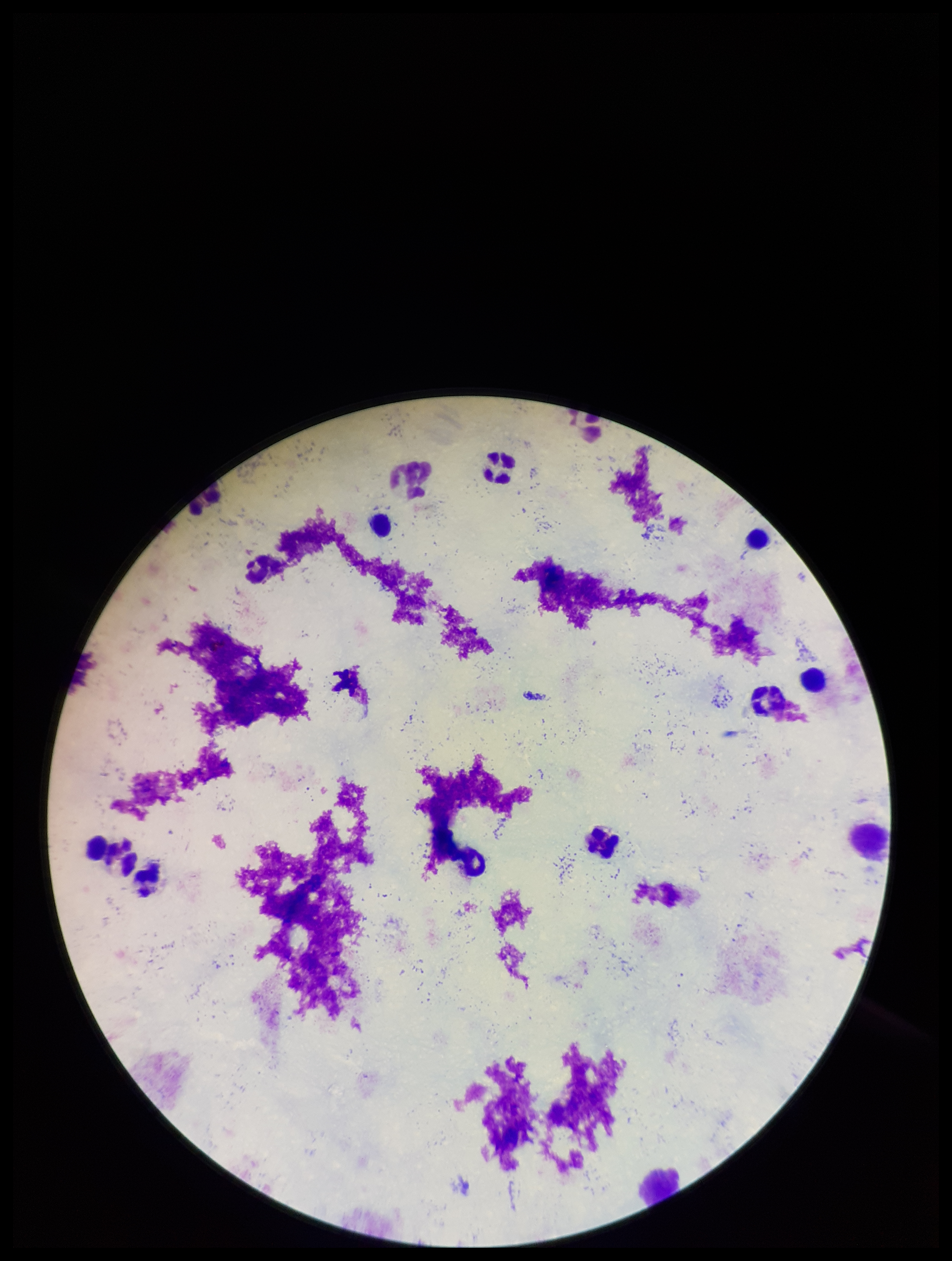
Summary:
  - Patient malaria status: negative
  - Image size: 952×1261 pixels
  - Preparation: thick blood smear
  - Leukocyte count: 10
  - Stain: Giemsa
  - Capture: smartphone photograph through the microscope eyepiece
  - Field of view: single
  - Plasmodium parasites: none detected
  - Parasite count: 0